Report the malaria status of this cell.
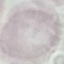
Uninfected.

Summary:
  - Preparation: thin blood smear
  - Capture: smartphone camera at the microscope eyepiece
  - Stain: Giemsa
  - Image type: automatically extracted cell patch, resized to 64 × 64 pixels